State the blood parasite species.
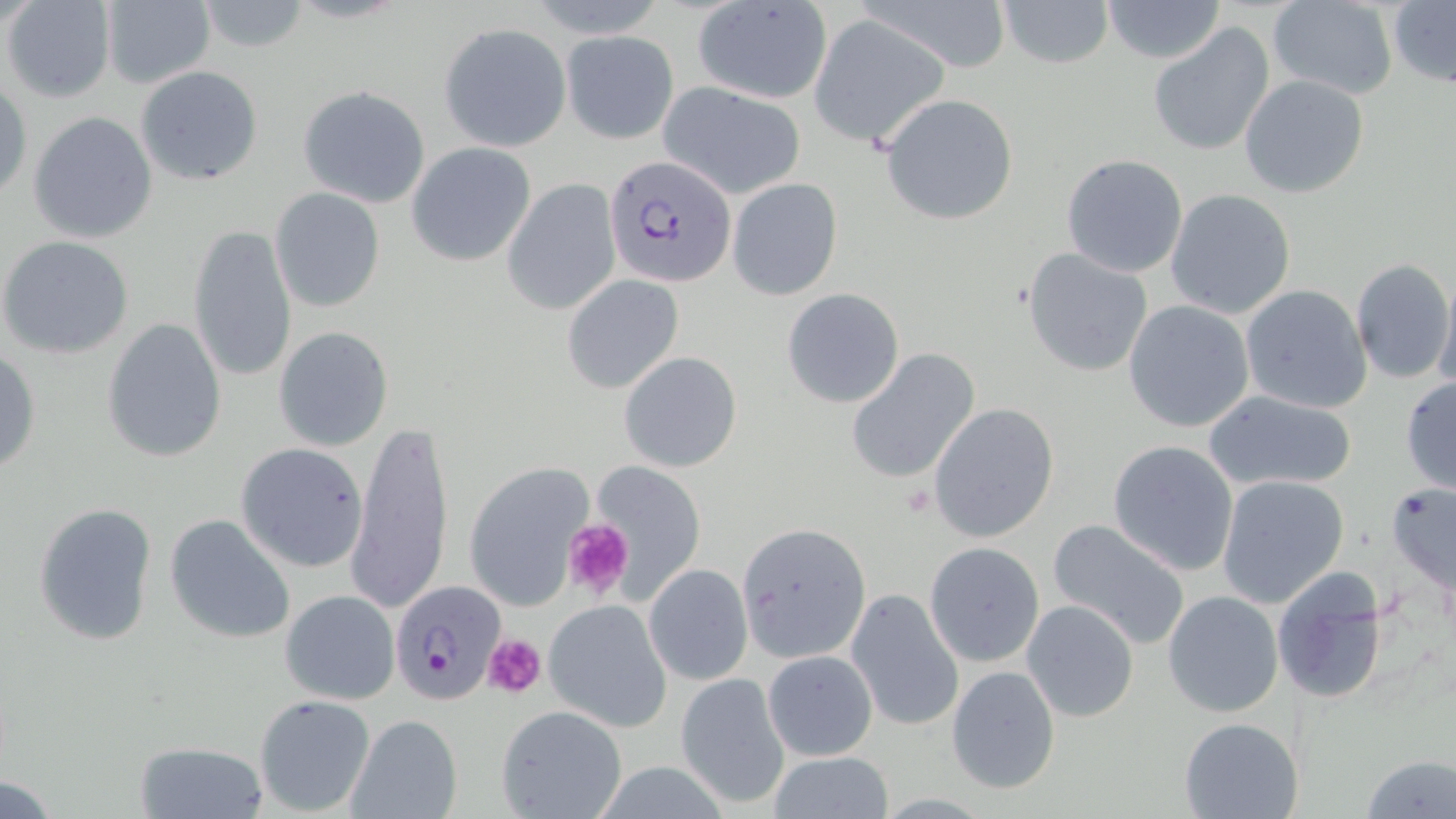
Plasmodium falciparum.

Approximate bounding boxes as (x1,y1)-(x2,y2) corner pairs in pixels. Plasmodium falciparum-infected red blood cell locations: (604,156)-(736,286), (390,580)-(505,705). Platelet locations: (561,517)-(636,603), (482,632)-(547,697). Uninfected red blood cell locations: (3,0)-(117,103), (859,0)-(1014,73), (995,0)-(1114,69), (1101,0)-(1226,64), (1266,0)-(1398,100), (99,1)-(216,88), (196,1)-(311,52), (691,1)-(834,105), (1388,1)-(1455,88), (808,15)-(950,148), (1147,20)-(1275,157), (438,23)-(570,152), (562,31)-(679,144), (136,65)-(262,187), (1239,74)-(1370,197), (1,80)-(30,202), (659,82)-(806,199), (297,85)-(433,209), (881,93)-(1019,225), (28,110)-(158,245), (407,143)-(536,266), (1060,153)-(1189,278), (728,177)-(841,299), (503,180)-(620,316), (270,187)-(385,313), (1164,188)-(1297,319), (187,223)-(297,383), (0,236)-(133,359), (1022,247)-(1152,376), (1350,256)-(1454,385), (1435,269)-(1456,396), (561,273)-(684,392), (1240,285)-(1373,413), (781,288)-(905,408), (1123,300)-(1256,433), (101,318)-(227,464), (273,326)-(394,451), (845,349)-(980,484), (0,350)-(41,475), (619,350)-(742,473), (1400,376)-(1456,495), (1205,389)-(1361,494), (927,402)-(1059,543), (346,418)-(454,617), (1107,439)-(1240,575), (235,442)-(370,574), (586,461)-(704,597), (464,462)-(594,610), (1217,476)-(1350,608), (1385,481)-(1456,599), (33,502)-(158,645), (164,513)-(295,645), (1047,517)-(1192,650), (925,542)-(1045,667), (644,564)-(752,685), (1270,566)-(1392,705), (845,587)-(964,733), (279,590)-(400,705), (1162,590)-(1285,718), (543,599)-(672,731), (1021,601)-(1140,722), (762,650)-(878,760), (946,664)-(1061,795), (674,671)-(791,811), (254,693)-(376,817), (496,705)-(628,819), (345,714)-(463,819), (1177,717)-(1305,819), (134,739)-(269,817), (765,752)-(893,819), (1360,754)-(1456,819), (2,776)-(60,817). Image is 1456×819 pixels. Light microscopy. Thin blood smear. One field of a larger specimen. May-Grünwald-Giemsa stain. 1000x magnification.